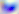
Summary:
  - Modality: micrograph
  - Magnification: 400x
  - Identification: Toxoplasma gondii